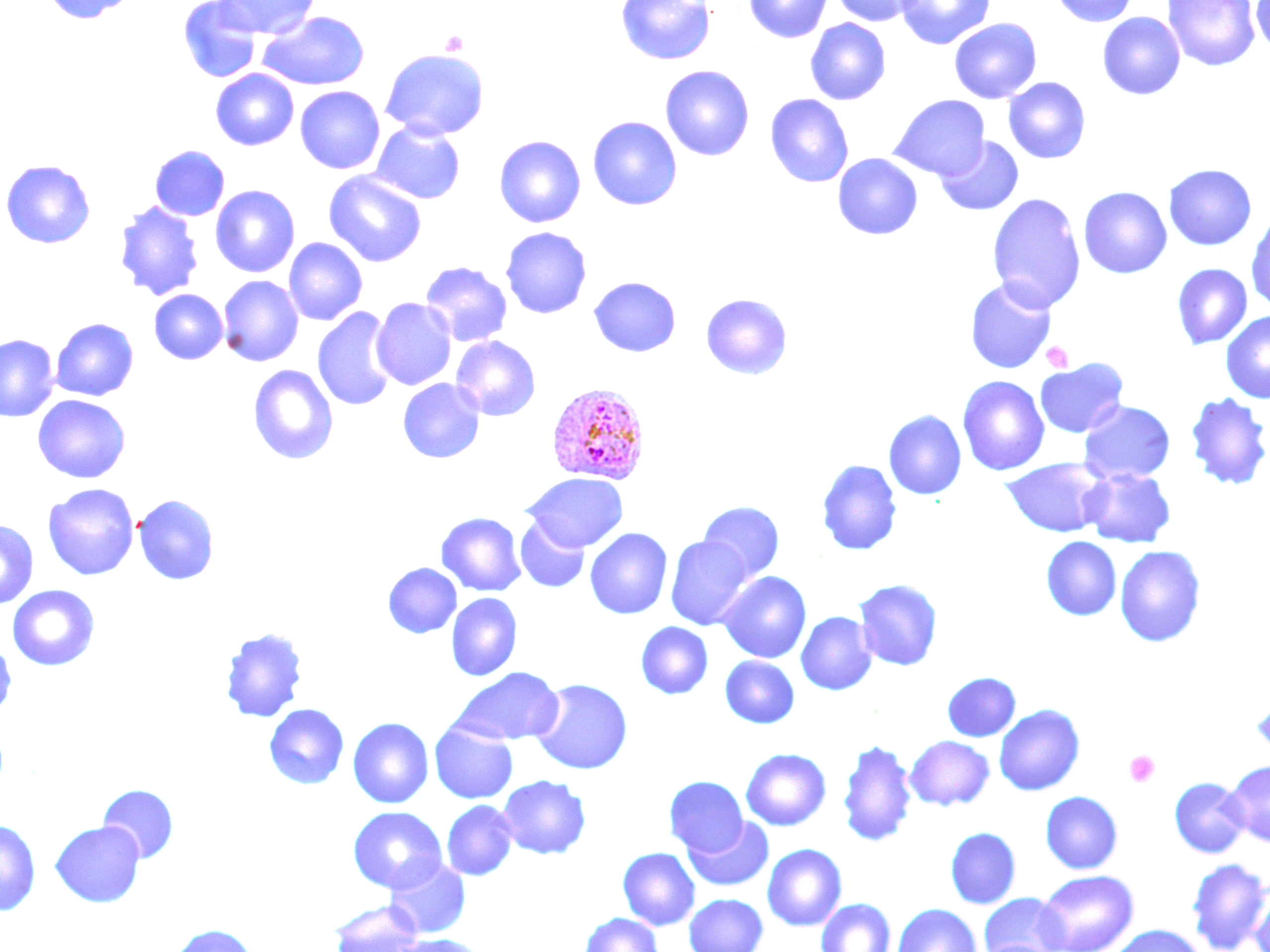

Summary:
  - Coordinate format: approximate bounding boxes as [x1, y1, x2, y2] in pixels
  - Platelet locations: [440, 30, 468, 55], [1042, 341, 1073, 372], [1124, 750, 1160, 787]
  - Uninfected red blood cell locations: [40, 0, 140, 24], [177, 0, 261, 83], [214, 0, 320, 38], [616, 0, 715, 65], [744, 0, 832, 43], [831, 0, 921, 26], [895, 0, 995, 50], [1049, 0, 1139, 27], [1163, 0, 1260, 72], [1251, 0, 1270, 56], [259, 11, 371, 91], [1097, 11, 1185, 100], [805, 18, 891, 105], [949, 18, 1042, 104], [380, 49, 489, 140], [660, 65, 755, 161], [211, 69, 298, 151], [1003, 77, 1091, 164], [295, 86, 384, 174], [765, 93, 854, 188], [889, 94, 990, 180], [588, 116, 682, 210], [371, 122, 465, 204], [494, 135, 585, 228], [935, 135, 1023, 216], [150, 145, 230, 221], [833, 153, 923, 240], [1, 159, 96, 249], [1163, 164, 1256, 250], [324, 171, 427, 267], [210, 185, 300, 278], [1078, 186, 1172, 279], [987, 193, 1086, 312], [114, 200, 204, 301], [1246, 212, 1270, 313], [500, 227, 592, 319], [284, 237, 367, 326], [419, 262, 512, 347], [1171, 263, 1252, 349], [218, 275, 304, 366], [588, 276, 681, 357], [965, 277, 1057, 373], [149, 289, 228, 364], [700, 293, 792, 379], [370, 297, 457, 390], [312, 307, 399, 413], [1220, 310, 1270, 403], [50, 317, 139, 401], [0, 334, 59, 421], [451, 336, 541, 421], [1035, 358, 1128, 438], [248, 364, 338, 465], [1051, 368, 1169, 457], [957, 375, 1050, 476], [398, 378, 485, 463], [1185, 391, 1270, 491], [33, 394, 131, 484], [1078, 399, 1175, 485], [884, 410, 967, 500], [1001, 458, 1110, 537], [817, 459, 901, 556], [1081, 468, 1175, 548], [523, 473, 627, 551], [42, 483, 139, 581], [133, 494, 219, 585], [698, 501, 784, 583], [436, 512, 526, 596], [514, 516, 590, 593], [0, 519, 39, 610], [585, 528, 672, 619], [666, 535, 754, 630], [1041, 536, 1121, 621], [1115, 545, 1206, 647], [383, 562, 461, 638], [718, 571, 811, 663], [853, 578, 942, 671], [7, 585, 100, 671], [446, 593, 522, 681], [796, 612, 877, 695], [636, 621, 713, 699], [220, 626, 308, 723], [0, 639, 16, 718], [720, 656, 799, 728], [451, 667, 564, 745], [942, 672, 1020, 741], [530, 678, 633, 775], [1250, 696, 1270, 761], [264, 704, 349, 789], [994, 704, 1084, 796], [348, 717, 434, 808], [429, 721, 518, 804], [904, 735, 994, 810], [837, 738, 917, 847], [741, 748, 831, 830], [1224, 760, 1270, 846], [497, 774, 591, 859], [664, 776, 748, 856], [1169, 777, 1249, 858], [97, 783, 179, 863], [1040, 791, 1123, 874], [441, 800, 518, 881], [347, 807, 447, 894], [684, 816, 774, 892], [0, 819, 41, 916], [50, 821, 145, 907], [945, 827, 1021, 909], [762, 844, 847, 930], [618, 847, 700, 930], [384, 857, 471, 938], [1186, 858, 1270, 952], [1036, 870, 1138, 952], [1248, 885, 1270, 952], [684, 893, 768, 952], [979, 893, 1070, 952], [816, 898, 895, 952], [329, 901, 424, 952], [892, 903, 981, 952], [579, 912, 664, 952], [168, 924, 259, 952], [1107, 925, 1206, 952], [390, 934, 486, 952]
  - Plasmodium vivax-infected red blood cell locations: [546, 382, 650, 485]
  - Slide-level diagnosis: Plasmodium vivax
  - Modality: light microscopy
  - Preparation: thin blood film
  - Stain: May-Grünwald-Giemsa
  - Image size: 1270×952 pixels
  - Magnification: 1000x
  - Field of view: single